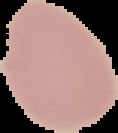

preparation = thin blood film
image size = 118×133 pixels
result = negative for malaria parasites
image type = segmented cell region on a black background